Comment on the morphology of the erythrocytes.
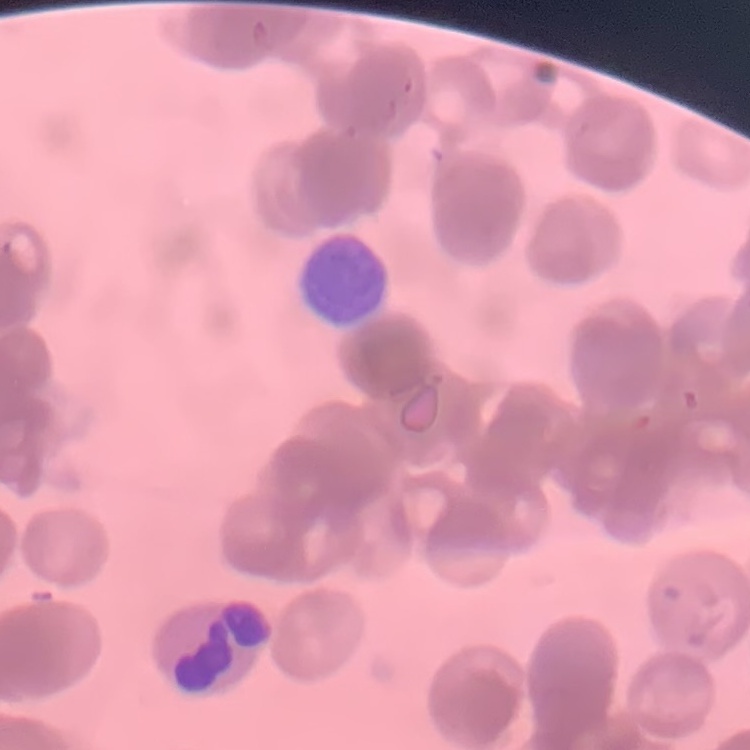

They show rouleaux formation.

Summary:
  - Image type: one tile cut from a larger photomicrograph
  - Stain: Field's or Giemsa
  - Preparation: thin blood film